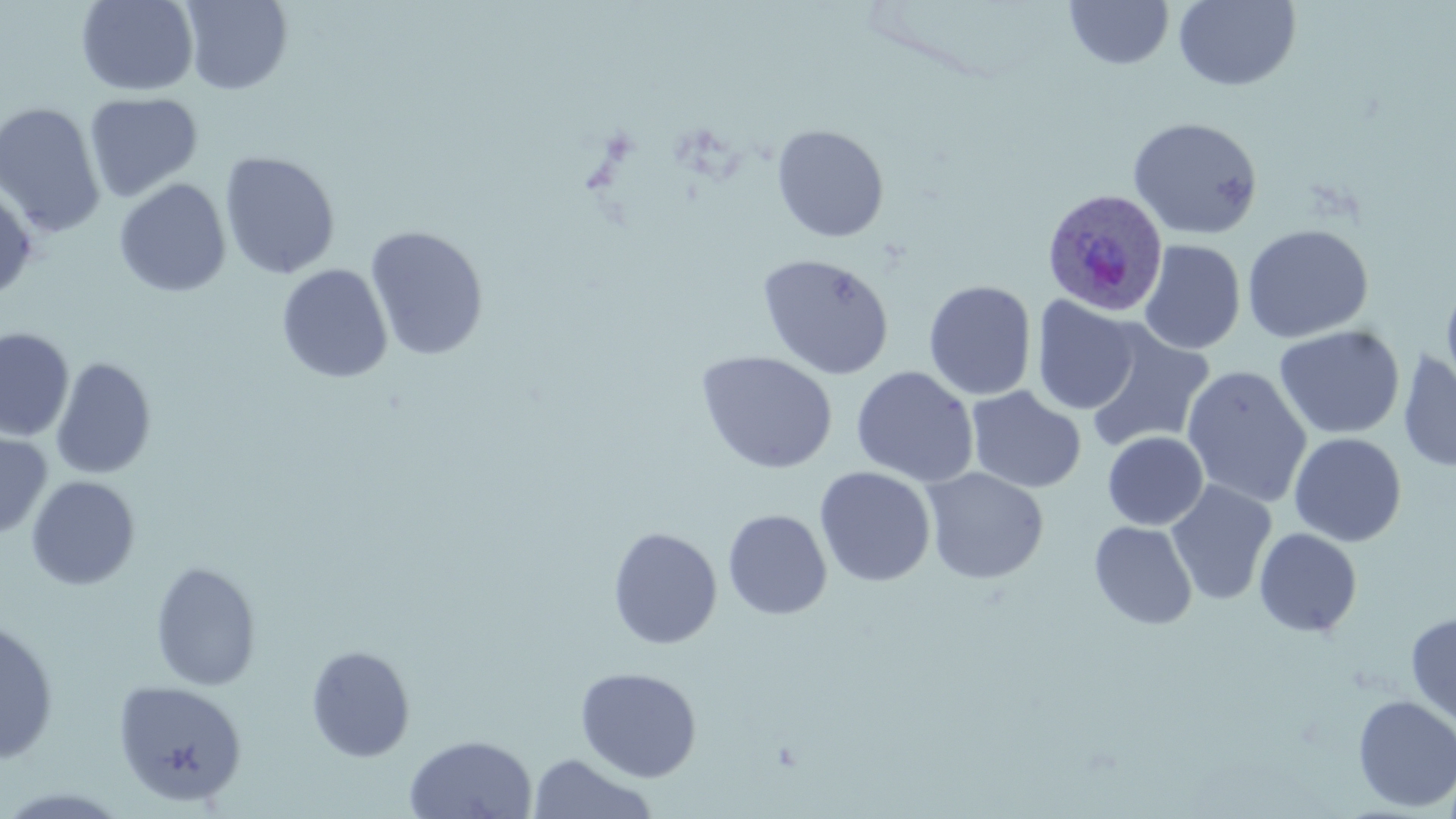 Approximate bounding boxes as named x1/y1/x2/y2 corners in pixels. Uninfected red blood cell locations: (x1=75, y1=0, x2=199, y2=96), (x1=180, y1=0, x2=293, y2=95), (x1=1173, y1=0, x2=1302, y2=92), (x1=1064, y1=1, x2=1174, y2=70), (x1=84, y1=92, x2=203, y2=203), (x1=0, y1=101, x2=106, y2=239), (x1=1127, y1=116, x2=1264, y2=240), (x1=771, y1=124, x2=890, y2=242), (x1=219, y1=151, x2=341, y2=280), (x1=114, y1=178, x2=231, y2=297), (x1=0, y1=180, x2=38, y2=299), (x1=1241, y1=223, x2=1374, y2=343), (x1=365, y1=225, x2=489, y2=361), (x1=1138, y1=239, x2=1246, y2=355), (x1=756, y1=253, x2=894, y2=380), (x1=276, y1=263, x2=393, y2=384), (x1=1441, y1=277, x2=1456, y2=400), (x1=923, y1=280, x2=1037, y2=400), (x1=1032, y1=296, x2=1141, y2=415), (x1=1083, y1=321, x2=1215, y2=455), (x1=1273, y1=325, x2=1405, y2=440), (x1=0, y1=327, x2=74, y2=442), (x1=695, y1=350, x2=838, y2=474), (x1=1397, y1=350, x2=1456, y2=472), (x1=50, y1=357, x2=157, y2=480), (x1=1180, y1=365, x2=1312, y2=508), (x1=850, y1=366, x2=979, y2=487), (x1=965, y1=386, x2=1087, y2=493), (x1=0, y1=428, x2=52, y2=541), (x1=1102, y1=431, x2=1208, y2=530), (x1=1288, y1=432, x2=1407, y2=547), (x1=814, y1=466, x2=937, y2=588), (x1=922, y1=467, x2=1049, y2=584), (x1=26, y1=475, x2=141, y2=590), (x1=1165, y1=479, x2=1278, y2=606), (x1=722, y1=509, x2=832, y2=620), (x1=1089, y1=521, x2=1198, y2=630), (x1=608, y1=526, x2=723, y2=649), (x1=1254, y1=527, x2=1363, y2=638), (x1=150, y1=560, x2=262, y2=691), (x1=1405, y1=612, x2=1456, y2=727), (x1=0, y1=619, x2=60, y2=764), (x1=305, y1=644, x2=416, y2=762), (x1=575, y1=666, x2=702, y2=782), (x1=113, y1=679, x2=247, y2=807), (x1=1352, y1=695, x2=1456, y2=812), (x1=403, y1=734, x2=538, y2=819), (x1=526, y1=753, x2=659, y2=819). Plasmodium ovale-infected red blood cell locations: (x1=1041, y1=187, x2=1169, y2=318). Slide-level diagnosis: Plasmodium ovale. Image is 1456×819 pixels. Light microscopy. Single field of view. May-Grünwald-Giemsa stain. Thin blood film. 1000x magnification.